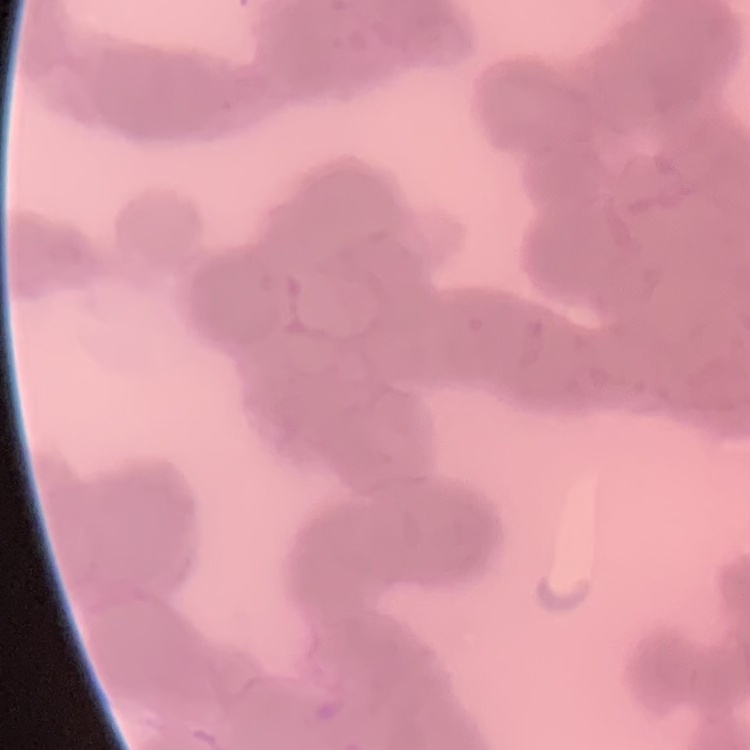

Summary:
  - Red blood cell morphology: rouleaux formation
  - Preparation: thin blood film
  - Stain: Field's or Giemsa
  - Image type: square crop of a larger photomicrograph